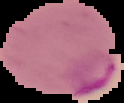

{
  "image_type": "segmented cell region on a black background",
  "preparation": "thin blood film",
  "image_size": "124×103 pixels",
  "result": "Plasmodium parasites identified"
}